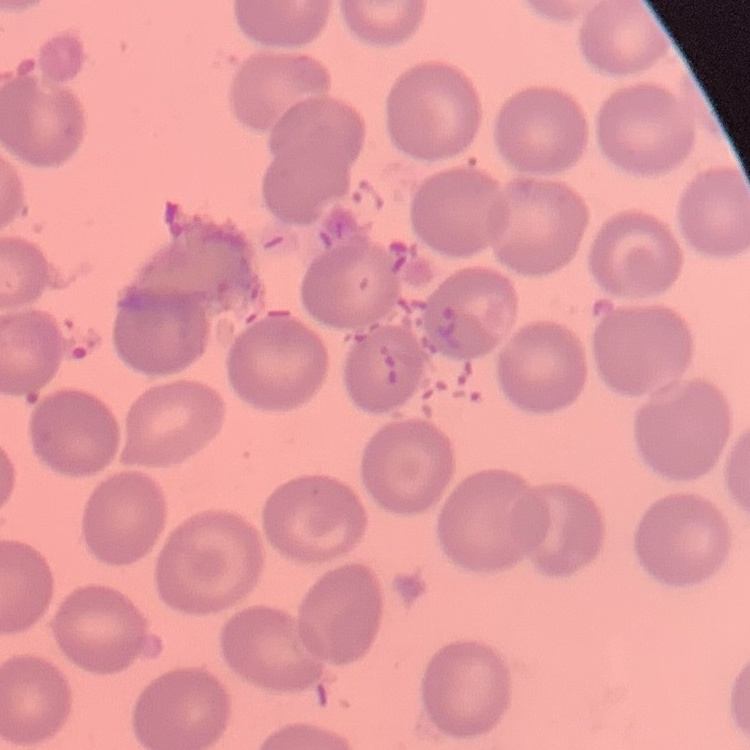 The red blood cells show no rouleaux formation. Stained with either Field's or Giemsa. One tile cut from a larger photomicrograph. Thin blood film.